Locate every uninfected red blood cell.
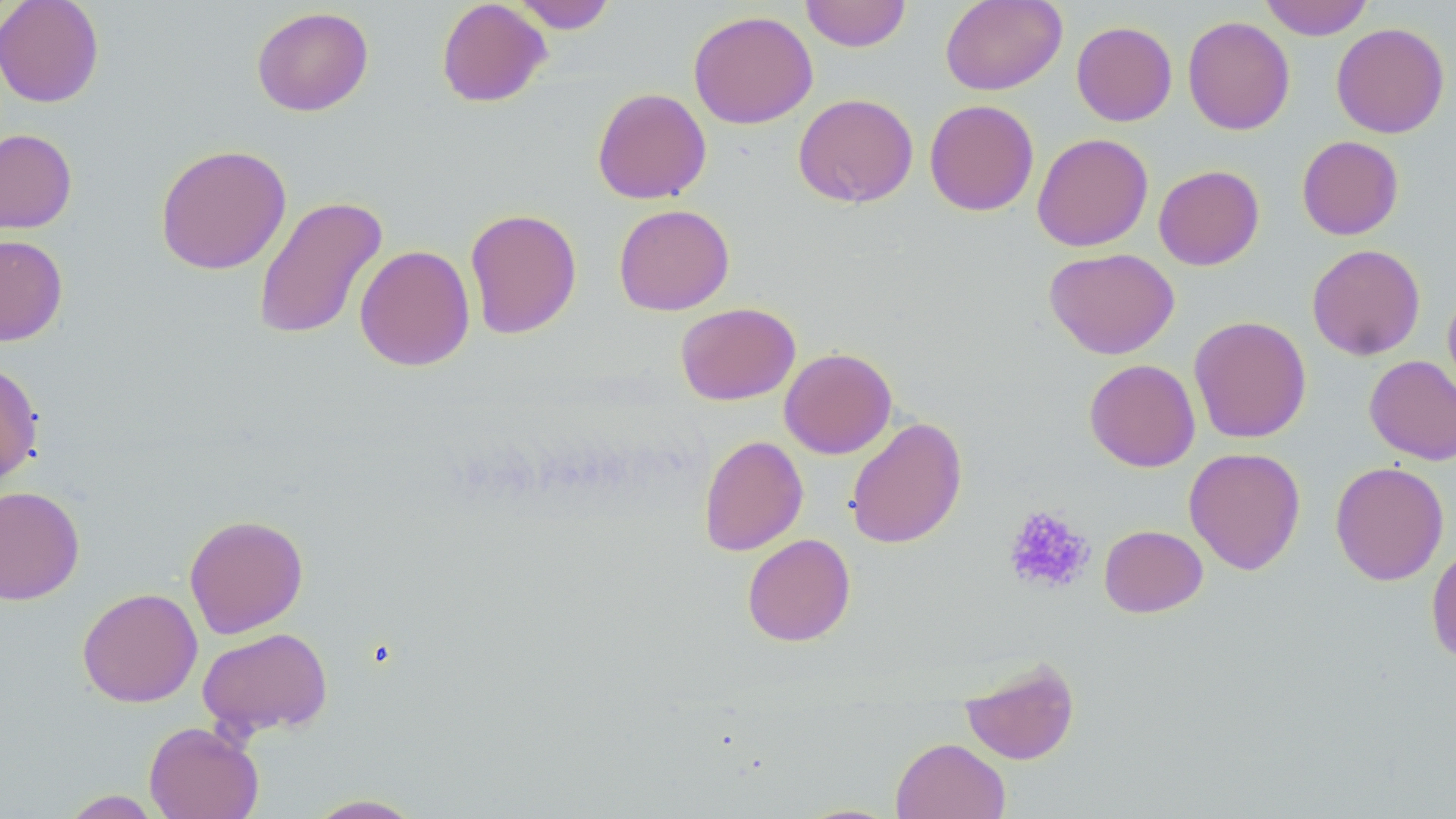
Approximate bounding boxes as (x1, y1, x2, y2) in pixels.
Uninfected red blood cells: (0, 0, 104, 108), (436, 0, 551, 108), (800, 0, 911, 52), (940, 0, 1067, 95), (1259, 0, 1373, 40), (510, 1, 617, 34), (252, 6, 374, 116), (688, 10, 818, 128), (1183, 15, 1295, 135), (1071, 21, 1177, 126), (1331, 22, 1450, 138), (592, 87, 711, 205), (793, 93, 919, 208), (924, 99, 1039, 216), (0, 128, 77, 234), (1032, 132, 1153, 252), (1297, 136, 1404, 240), (154, 144, 291, 275), (1153, 165, 1264, 270), (252, 194, 388, 341), (613, 203, 734, 316), (464, 207, 582, 340), (0, 235, 68, 346), (1307, 243, 1426, 360), (354, 244, 475, 371), (1044, 247, 1179, 359), (1442, 288, 1456, 403), (675, 302, 800, 405), (1189, 315, 1311, 443), (779, 347, 896, 459), (1364, 355, 1456, 465), (1084, 359, 1200, 472), (0, 361, 43, 486), (845, 416, 967, 549), (698, 434, 808, 556), (1184, 447, 1306, 575), (1330, 461, 1450, 586), (0, 485, 85, 605), (184, 514, 308, 638), (1099, 524, 1208, 617), (742, 533, 856, 646), (1426, 542, 1456, 664), (77, 587, 202, 707), (197, 626, 333, 738), (960, 656, 1080, 765), (143, 721, 264, 819), (891, 737, 1010, 819), (60, 790, 164, 818), (305, 794, 427, 818), (791, 802, 905, 818).

Platelet locations: (1003, 505, 1094, 596). Slide-level diagnosis: no evidence of blood parasites. Captured at 1000x magnification. Optical microscopy. Thin blood film. May-Grünwald-Giemsa stain. Image is 1456×819 pixels. One field of a larger specimen.